Point out every malaria parasite and every leukocyte.
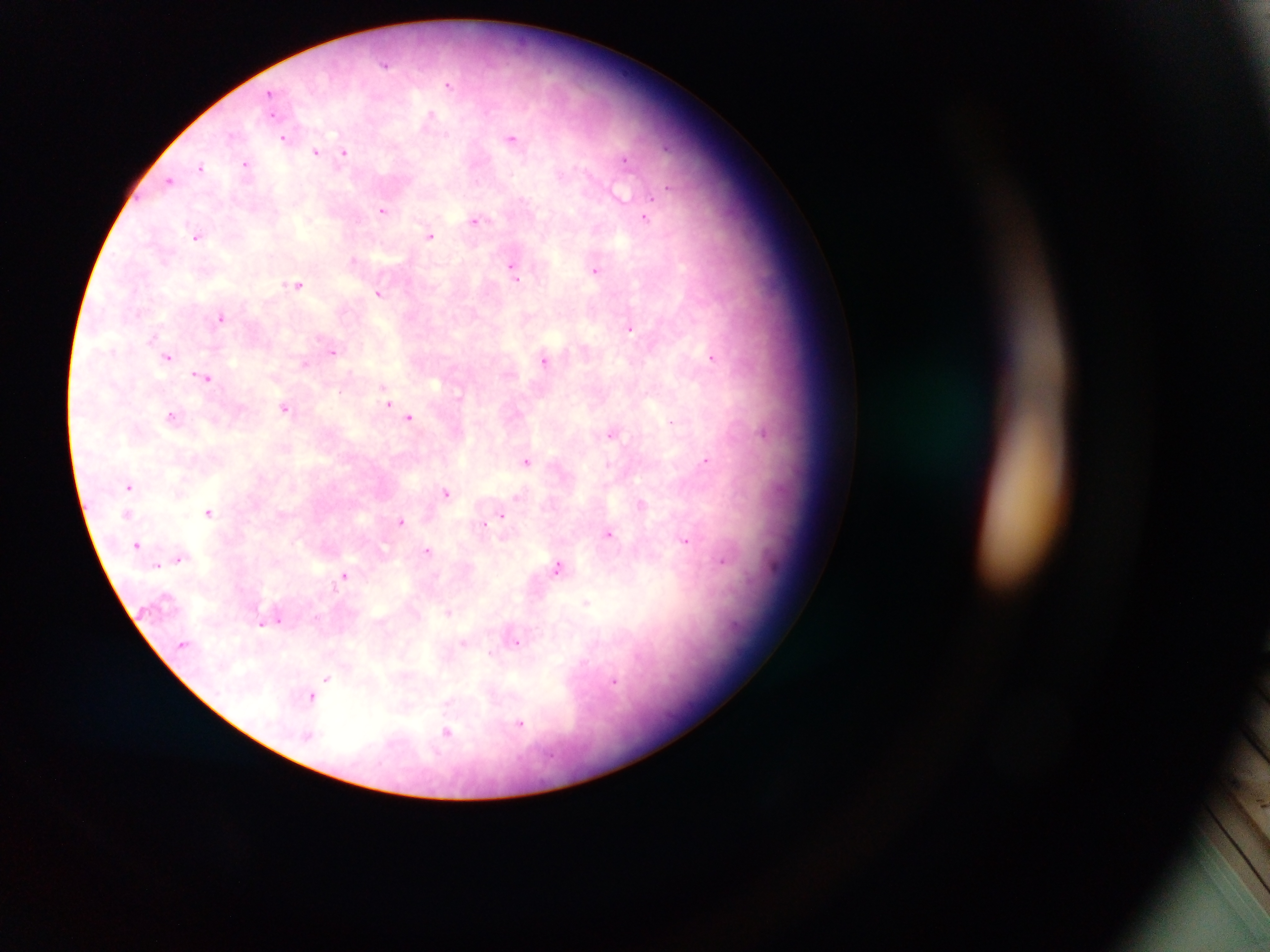
Approximate centers as (x, y) in pixels.
Malaria parasites: (386, 65), (450, 83), (271, 94), (431, 117), (513, 137), (284, 138), (316, 152), (345, 152), (626, 160), (246, 163), (201, 168), (170, 180), (652, 195), (383, 209), (646, 218), (477, 220), (430, 235), (197, 236), (354, 259), (515, 268), (596, 269), (299, 284), (379, 293), (221, 317), (630, 328), (585, 350), (333, 351), (169, 356), (712, 356), (544, 360), (305, 362), (204, 376), (389, 403), (285, 405), (173, 415), (411, 417), (671, 422), (613, 431), (765, 432), (705, 460), (528, 461), (606, 464), (130, 486), (447, 492), (641, 502), (209, 511), (501, 514), (401, 521), (484, 523), (609, 534), (687, 541), (137, 543), (427, 551), (179, 557), (723, 560), (559, 566), (345, 575), (586, 603), (448, 611), (278, 619), (263, 621), (516, 641), (464, 644), (327, 678), (613, 679), (325, 684), (313, 695), (521, 723), (448, 731).
No leukocytes observed.

Photographed through a microscope with a mobile-phone camera. One field of view. Collected in Ghana. Thick blood smear. Image is 1270×952 pixels.